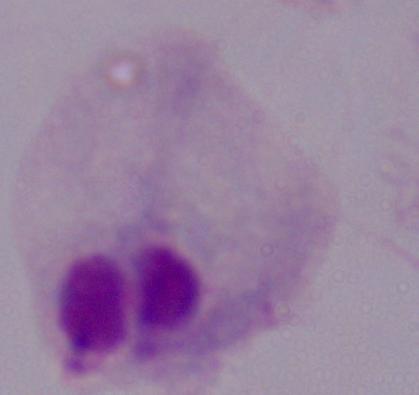

Photomicrograph. A trichomonad is shown. Captured at 1000x magnification.